State the blood parasite species.
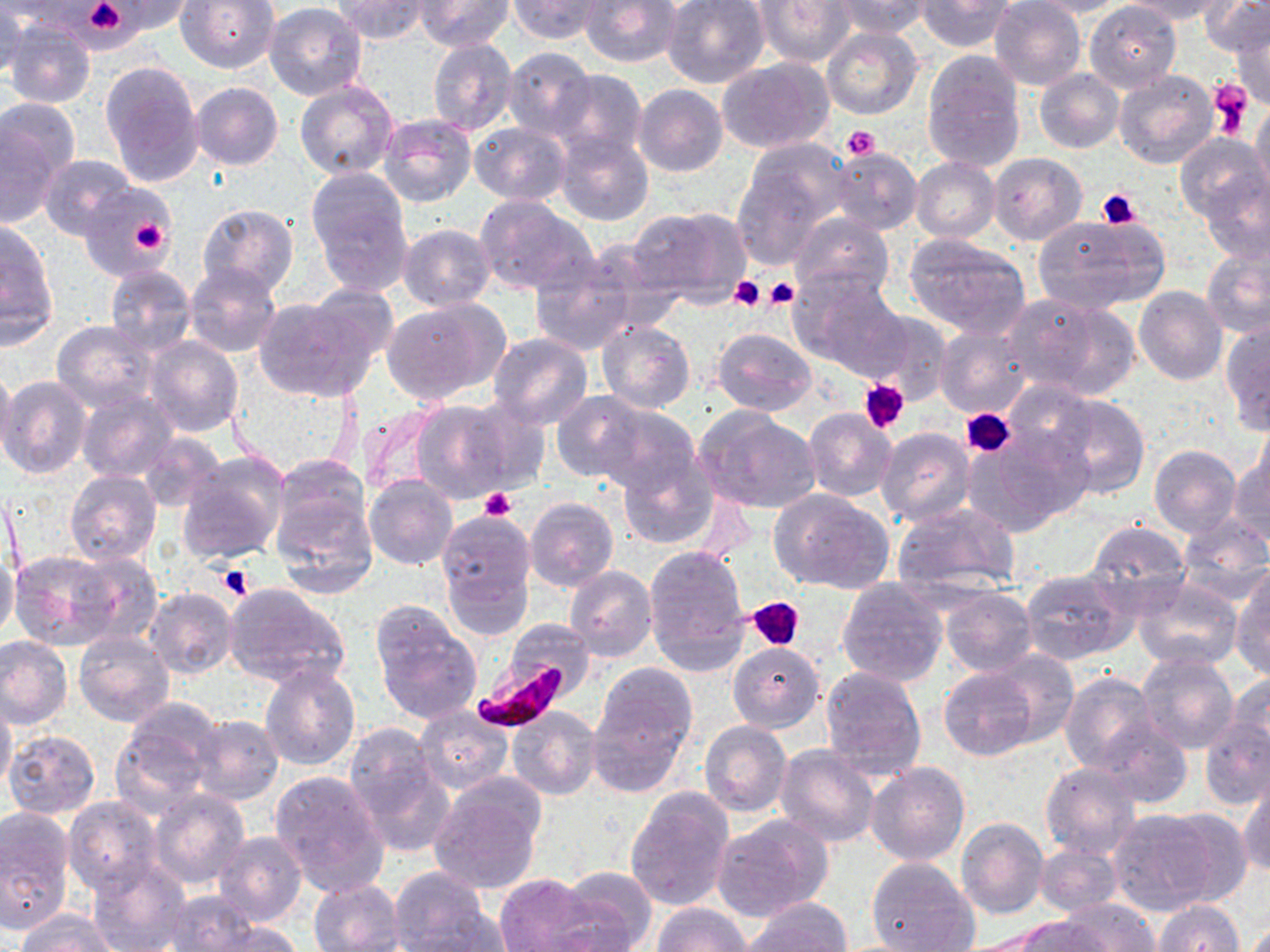
Plasmodium falciparum.

stain = May-Grünwald-Giemsa
preparation = thin blood film
modality = light microscopy
field of view = single
magnification = 1000x
uninfected red blood cell locations = approximate bounding boxes as named x1/y1/x2/y2 corners in pixels: (x1=100, y1=0, x2=195, y2=36), (x1=178, y1=0, x2=280, y2=73), (x1=333, y1=0, x2=431, y2=43), (x1=416, y1=0, x2=513, y2=50), (x1=507, y1=0, x2=609, y2=43), (x1=578, y1=0, x2=682, y2=69), (x1=661, y1=0, x2=771, y2=89), (x1=754, y1=0, x2=856, y2=67), (x1=831, y1=0, x2=931, y2=38), (x1=989, y1=0, x2=1086, y2=90), (x1=1022, y1=0, x2=1126, y2=18), (x1=1126, y1=0, x2=1232, y2=22), (x1=1201, y1=0, x2=1269, y2=56), (x1=915, y1=1, x2=1016, y2=52), (x1=0, y1=2, x2=24, y2=85), (x1=263, y1=2, x2=367, y2=100), (x1=1085, y1=2, x2=1182, y2=93), (x1=4, y1=18, x2=95, y2=108), (x1=1227, y1=18, x2=1270, y2=107), (x1=821, y1=27, x2=923, y2=120), (x1=427, y1=37, x2=518, y2=137), (x1=501, y1=48, x2=597, y2=140), (x1=920, y1=53, x2=1026, y2=173), (x1=718, y1=59, x2=831, y2=154), (x1=100, y1=61, x2=205, y2=187), (x1=1113, y1=68, x2=1218, y2=169), (x1=552, y1=69, x2=647, y2=162), (x1=1034, y1=69, x2=1123, y2=153), (x1=294, y1=80, x2=399, y2=181), (x1=190, y1=82, x2=284, y2=170), (x1=633, y1=84, x2=727, y2=177), (x1=1251, y1=97, x2=1270, y2=201), (x1=2, y1=98, x2=81, y2=188), (x1=378, y1=113, x2=477, y2=207), (x1=0, y1=119, x2=65, y2=227), (x1=468, y1=122, x2=571, y2=205), (x1=552, y1=130, x2=653, y2=227), (x1=1174, y1=132, x2=1269, y2=224), (x1=734, y1=139, x2=850, y2=263), (x1=830, y1=147, x2=922, y2=235), (x1=989, y1=152, x2=1086, y2=244), (x1=38, y1=153, x2=135, y2=239), (x1=910, y1=157, x2=1000, y2=242), (x1=1200, y1=167, x2=1270, y2=264), (x1=306, y1=169, x2=413, y2=293), (x1=80, y1=182, x2=179, y2=281), (x1=474, y1=195, x2=597, y2=298), (x1=197, y1=204, x2=299, y2=296), (x1=629, y1=205, x2=752, y2=308), (x1=790, y1=211, x2=893, y2=302), (x1=1031, y1=214, x2=1163, y2=316), (x1=1, y1=220, x2=59, y2=345), (x1=398, y1=223, x2=496, y2=310), (x1=905, y1=234, x2=1031, y2=337), (x1=1201, y1=245, x2=1270, y2=339), (x1=528, y1=252, x2=643, y2=356), (x1=185, y1=262, x2=281, y2=358), (x1=104, y1=264, x2=196, y2=355), (x1=791, y1=269, x2=908, y2=376), (x1=309, y1=284, x2=401, y2=366), (x1=1134, y1=287, x2=1227, y2=386), (x1=1003, y1=294, x2=1135, y2=398), (x1=253, y1=296, x2=375, y2=401), (x1=383, y1=298, x2=509, y2=403), (x1=864, y1=311, x2=953, y2=404), (x1=596, y1=320, x2=694, y2=413), (x1=53, y1=321, x2=157, y2=411), (x1=1220, y1=322, x2=1270, y2=437), (x1=934, y1=324, x2=1032, y2=420), (x1=712, y1=327, x2=818, y2=415), (x1=488, y1=333, x2=594, y2=430), (x1=146, y1=336, x2=243, y2=437), (x1=0, y1=364, x2=16, y2=468), (x1=1, y1=376, x2=92, y2=479), (x1=76, y1=389, x2=177, y2=482), (x1=551, y1=391, x2=652, y2=485), (x1=1044, y1=391, x2=1150, y2=499), (x1=455, y1=395, x2=554, y2=494), (x1=409, y1=400, x2=514, y2=502), (x1=591, y1=404, x2=702, y2=500), (x1=804, y1=408, x2=896, y2=501), (x1=693, y1=409, x2=820, y2=513), (x1=877, y1=429, x2=976, y2=527), (x1=966, y1=429, x2=1086, y2=535), (x1=139, y1=432, x2=225, y2=512), (x1=1149, y1=445, x2=1241, y2=539), (x1=616, y1=450, x2=720, y2=548), (x1=177, y1=452, x2=290, y2=565), (x1=1229, y1=452, x2=1270, y2=548), (x1=270, y1=454, x2=370, y2=552), (x1=65, y1=471, x2=161, y2=566), (x1=363, y1=474, x2=457, y2=570), (x1=3, y1=481, x2=23, y2=583), (x1=270, y1=486, x2=378, y2=600), (x1=770, y1=488, x2=895, y2=597), (x1=525, y1=497, x2=619, y2=592), (x1=891, y1=503, x2=1020, y2=600), (x1=436, y1=510, x2=535, y2=632), (x1=1175, y1=515, x2=1270, y2=606), (x1=1085, y1=520, x2=1193, y2=615), (x1=643, y1=545, x2=751, y2=673), (x1=71, y1=549, x2=165, y2=647), (x1=0, y1=551, x2=20, y2=644), (x1=10, y1=551, x2=121, y2=650), (x1=564, y1=566, x2=656, y2=662), (x1=1020, y1=568, x2=1134, y2=663), (x1=1232, y1=570, x2=1270, y2=680), (x1=1132, y1=576, x2=1242, y2=672), (x1=836, y1=577, x2=948, y2=687), (x1=224, y1=586, x2=350, y2=688), (x1=940, y1=586, x2=1038, y2=676), (x1=146, y1=588, x2=240, y2=679), (x1=373, y1=608, x2=481, y2=722), (x1=505, y1=621, x2=595, y2=696), (x1=74, y1=630, x2=174, y2=726), (x1=0, y1=636, x2=73, y2=730), (x1=727, y1=642, x2=825, y2=733), (x1=983, y1=652, x2=1080, y2=746), (x1=1133, y1=653, x2=1239, y2=754), (x1=259, y1=663, x2=361, y2=772), (x1=589, y1=663, x2=697, y2=780), (x1=819, y1=665, x2=928, y2=777), (x1=940, y1=669, x2=1036, y2=761), (x1=1059, y1=671, x2=1160, y2=776), (x1=1227, y1=673, x2=1270, y2=767), (x1=0, y1=696, x2=17, y2=794), (x1=112, y1=706, x2=216, y2=813), (x1=415, y1=706, x2=513, y2=795), (x1=507, y1=707, x2=603, y2=799), (x1=192, y1=715, x2=284, y2=804), (x1=1200, y1=718, x2=1270, y2=811), (x1=1096, y1=719, x2=1193, y2=808), (x1=699, y1=721, x2=792, y2=817), (x1=344, y1=725, x2=452, y2=851), (x1=3, y1=729, x2=101, y2=820), (x1=775, y1=745, x2=881, y2=847), (x1=865, y1=762, x2=969, y2=866), (x1=1040, y1=763, x2=1141, y2=861), (x1=269, y1=769, x2=390, y2=896), (x1=1239, y1=778, x2=1270, y2=879), (x1=429, y1=779, x2=546, y2=894), (x1=624, y1=788, x2=735, y2=911), (x1=149, y1=789, x2=249, y2=887), (x1=63, y1=798, x2=165, y2=895), (x1=1149, y1=805, x2=1253, y2=904), (x1=0, y1=806, x2=75, y2=936), (x1=1106, y1=810, x2=1221, y2=916), (x1=711, y1=814, x2=833, y2=921), (x1=955, y1=817, x2=1049, y2=921), (x1=214, y1=832, x2=307, y2=926), (x1=1036, y1=844, x2=1123, y2=915), (x1=85, y1=856, x2=191, y2=952), (x1=866, y1=856, x2=979, y2=952), (x1=557, y1=865, x2=657, y2=950), (x1=388, y1=867, x2=493, y2=951), (x1=495, y1=872, x2=599, y2=952), (x1=308, y1=879, x2=405, y2=951), (x1=162, y1=891, x2=266, y2=951), (x1=1060, y1=898, x2=1161, y2=952), (x1=744, y1=899, x2=852, y2=952), (x1=1153, y1=900, x2=1244, y2=952), (x1=653, y1=903, x2=752, y2=952), (x1=410, y1=908, x2=514, y2=949), (x1=16, y1=909, x2=115, y2=952), (x1=1013, y1=914, x2=1109, y2=952), (x1=198, y1=918, x2=302, y2=951)
image size = 1270×952 pixels
Plasmodium falciparum-infected red blood cell locations = approximate bounding boxes as named x1/y1/x2/y2 corners in pixels: (x1=474, y1=657, x2=572, y2=732)
platelet locations = approximate bounding boxes as named x1/y1/x2/y2 corners in pixels: (x1=79, y1=0, x2=135, y2=41), (x1=1208, y1=76, x2=1251, y2=137), (x1=842, y1=126, x2=879, y2=161), (x1=1097, y1=189, x2=1140, y2=229), (x1=129, y1=214, x2=171, y2=255), (x1=730, y1=276, x2=765, y2=312), (x1=764, y1=278, x2=797, y2=310), (x1=861, y1=380, x2=910, y2=433), (x1=961, y1=409, x2=1014, y2=457), (x1=480, y1=487, x2=515, y2=520), (x1=217, y1=564, x2=255, y2=601), (x1=748, y1=596, x2=804, y2=651)